Describe the morphology of the erythrocytes.
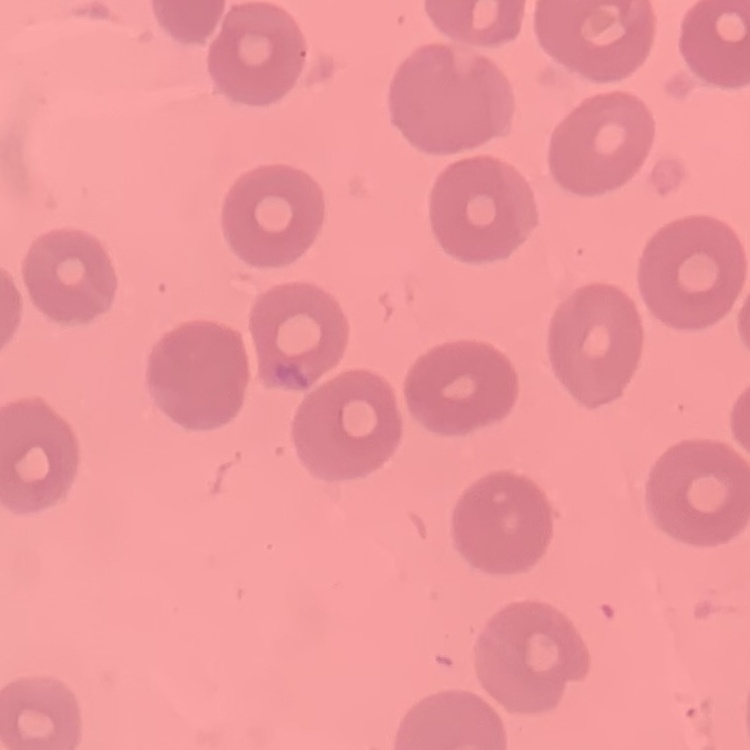
No rouleaux formation.

Summary:
  - Stain: Field's or Giemsa
  - Image type: square crop of a larger photomicrograph
  - Preparation: thin peripheral smear